Describe the morphology of the red blood cells.
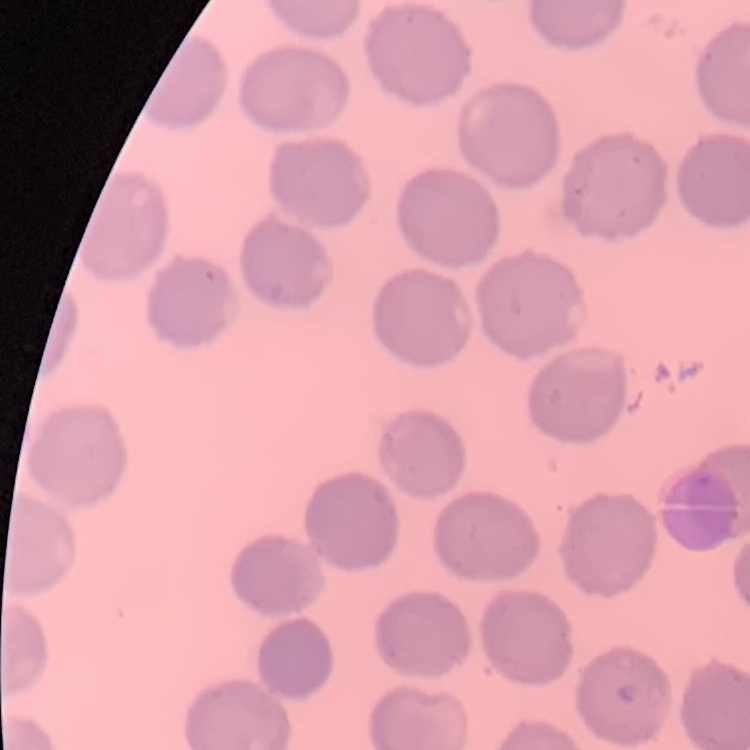

They show no rouleaux formation.

Summary:
  - Preparation: thin blood film
  - Stain: Field's or Giemsa
  - Image type: one tile cut from a larger photomicrograph